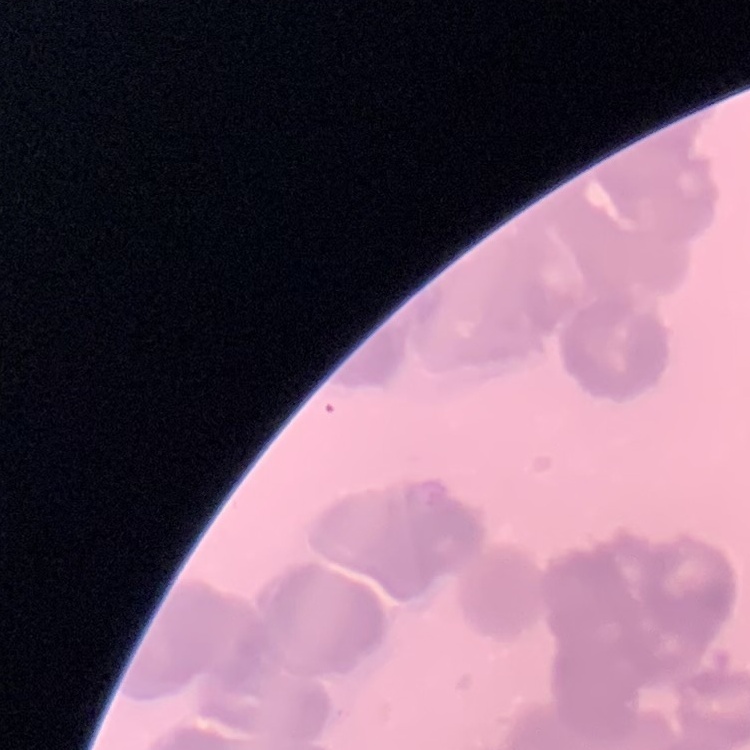
red blood cell morphology = rouleaux formation
stain = Field's or Giemsa
preparation = thin peripheral smear
image type = square crop of a larger photomicrograph